Report the malaria status of this cell.
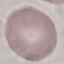
Uninfected.

Summary:
  - Preparation: thin blood film
  - Capture: smartphone camera at the microscope eyepiece
  - Stain: Giemsa
  - Image type: automatically extracted cell patch, resized to 64 × 64 pixels